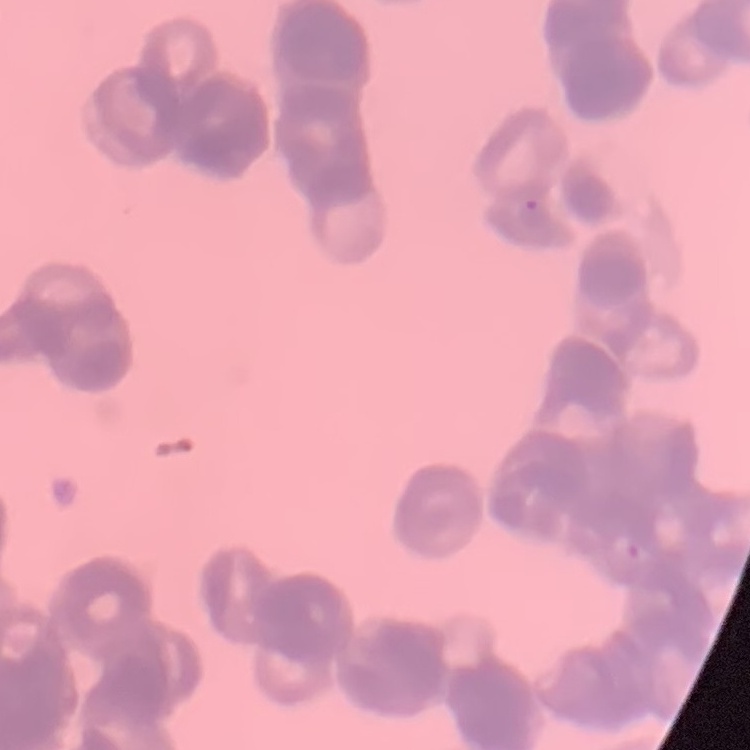 The red blood cells show rouleaux formation. Thin peripheral smear. One tile cut from a larger photomicrograph. Stained with either Field's or Giemsa.